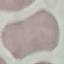

Result: no malaria parasites seen. Acquired by smartphone through the microscope eyepiece. Thin smear of blood. Cell patch, automatically extracted from a larger field of view and resized to 64 × 64 pixels. Giemsa-stained preparation.